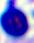

magnification = 400x
modality = photomicrograph
identification = white blood cell